Assess this cell for malaria.
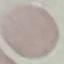
It is uninfected.

Acquired by smartphone through the microscope eyepiece. Thin smear of blood. Giemsa-stained preparation. Cell patch, automatically extracted from a larger field of view and resized to 64 × 64 pixels.